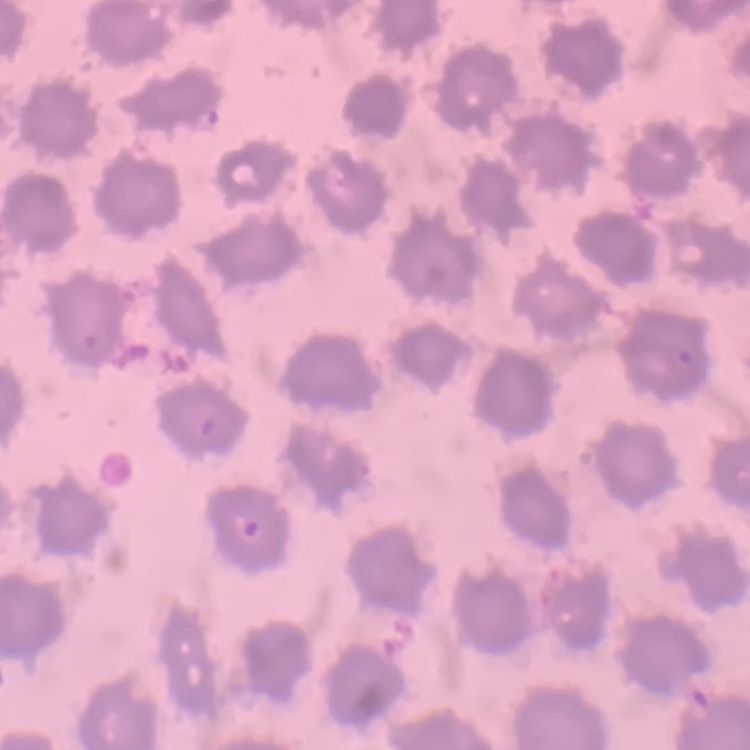

red_blood_cell_morphology: no rouleaux formation
image_type: one tile cut from a larger photomicrograph
stain: Field's or Giemsa
preparation: thin peripheral smear